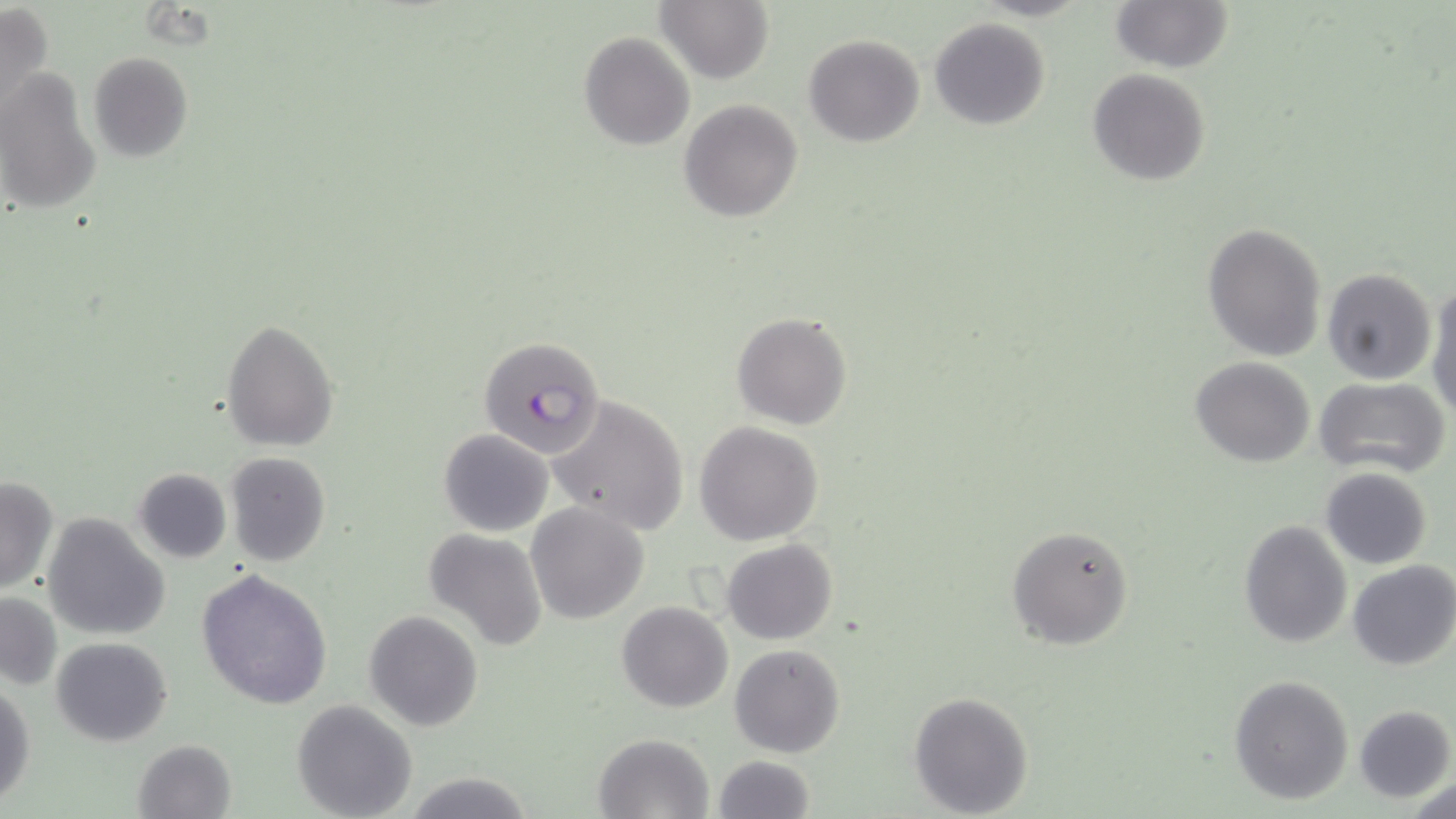
Summary:
  - Coordinate format: approximate bounding boxes as (x1,y1)-(x2,y2) corner pairs in pixels
  - Uninfected red blood cell locations: (0,0)-(56,128), (1110,0)-(1233,74), (656,2)-(773,84), (930,16)-(1051,130), (579,31)-(695,150), (803,33)-(924,147), (87,51)-(193,162), (1088,68)-(1212,186), (1,71)-(103,218), (678,98)-(803,221), (1201,222)-(1328,362), (1322,268)-(1436,385), (1426,281)-(1456,419), (731,311)-(852,430), (220,320)-(339,450), (1191,356)-(1315,467), (1314,376)-(1451,479), (547,393)-(690,534), (693,420)-(824,546), (438,428)-(553,536), (224,451)-(331,566), (133,467)-(232,564), (1320,467)-(1433,569), (0,476)-(57,596), (526,502)-(650,624), (41,515)-(172,640), (1239,518)-(1353,649), (1006,524)-(1135,649), (423,528)-(547,650), (721,538)-(838,644), (1347,560)-(1456,671), (196,568)-(333,709), (0,592)-(63,692), (616,601)-(734,713), (364,609)-(484,731), (52,637)-(172,747), (729,643)-(845,758), (1229,674)-(1354,805), (0,685)-(35,807), (906,690)-(1034,817), (292,700)-(419,819), (1354,704)-(1455,802), (593,733)-(713,819), (132,738)-(238,819), (712,755)-(816,819), (401,769)-(534,819), (1407,776)-(1455,819)
  - Plasmodium falciparum-infected red blood cell locations: (479,336)-(609,460)
  - Slide-level diagnosis: Plasmodium falciparum
  - Magnification: 1000x
  - Image size: 1456×819 pixels
  - Field of view: single
  - Stain: May-Grünwald-Giemsa
  - Modality: optical microscopy
  - Preparation: thin blood film